Describe the morphology of the erythrocytes.
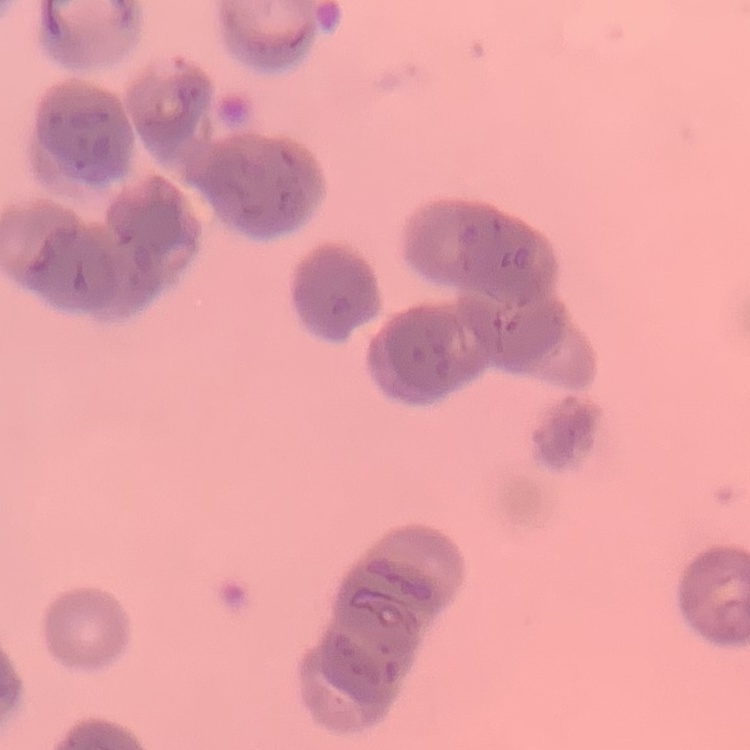

They show rouleaux formation.

Summary:
  - Image type: square crop of a larger photomicrograph
  - Stain: Field's or Giemsa
  - Preparation: thin peripheral smear